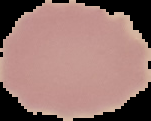
Summary:
  - Image type: segmented cell region on a black background
  - Malaria status: uninfected
  - Image size: 151×121 pixels
  - Preparation: thin blood film